Comment on the morphology of the red blood cells.
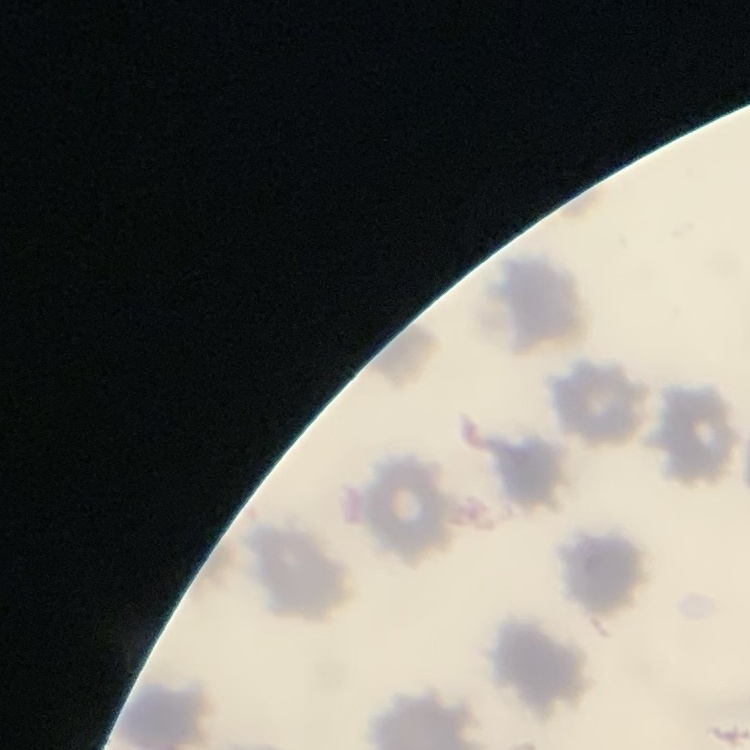

They show no rouleaux formation.

Stained with either Field's or Giemsa. Thin peripheral smear. Square crop of a larger photomicrograph.